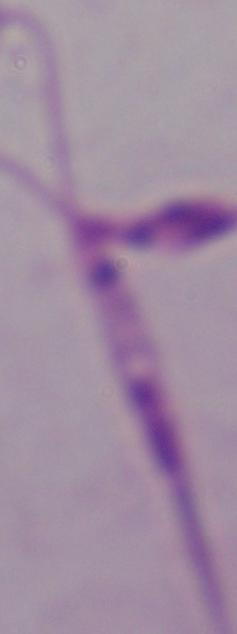
identification = Leishmania
magnification = 1000x
modality = micrograph